Assess the morphology of the erythrocytes.
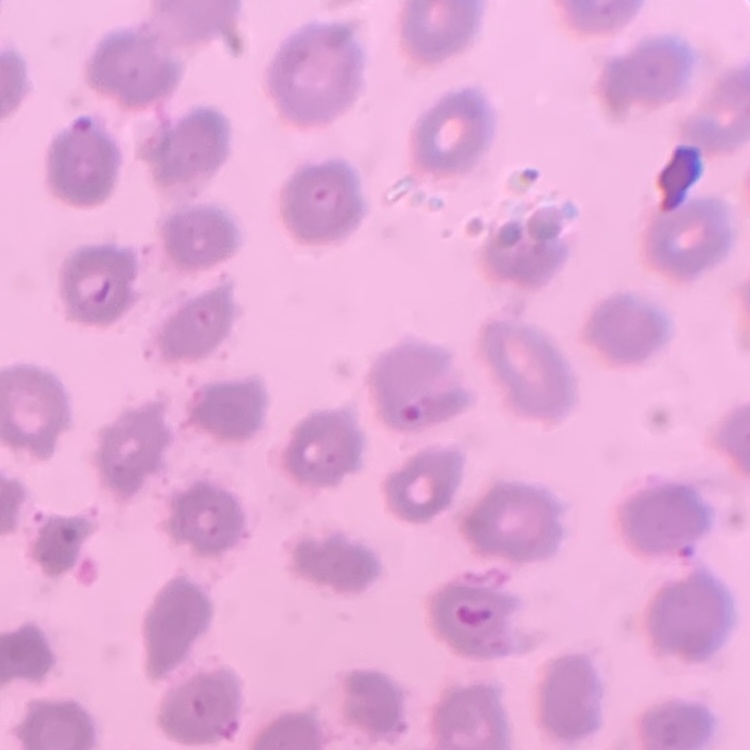
No rouleaux formation.

stain = Field's or Giemsa
image type = one tile cut from a larger photomicrograph
preparation = thin blood film